Classify this cell by malaria status.
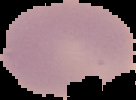
Uninfected.

Segmented cell region on a black background. From a thin blood smear. Image is 136×100 pixels.